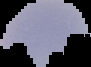 Image is 91×67 pixels. Cell region segmented out of the field of view; the surrounding area is masked to black. From a thin blood film. Result: no malaria parasites seen.